State which cell type is depicted.
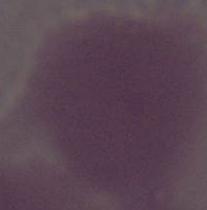

An erythrocyte.

Summary:
  - Magnification: 1000x
  - Modality: micrograph